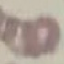

result = no malaria parasites detected
image type = automatically extracted cell patch, resized to 64 × 64 pixels
preparation = thin blood smear
stain = Giemsa
capture = smartphone camera at the microscope eyepiece